Report the malaria status of this cell.
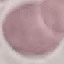

It is uninfected.

Summary:
  - Stain: Giemsa
  - Capture: smartphone camera at the microscope eyepiece
  - Image type: automatically extracted cell patch, resized to 64 × 64 pixels
  - Preparation: thin blood smear